Report the malaria status of this cell.
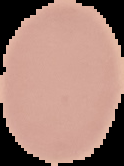

Uninfected.

Summary:
  - Preparation: thin blood smear
  - Image size: 124×166 pixels
  - Image type: segmented cell region on a black background